Classify this cell by malaria status.
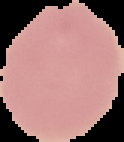

It is uninfected.

From a thin blood film. Segmented cell region on a black background. Image is 124×142 pixels.